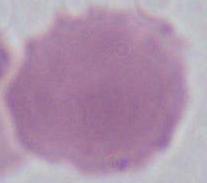
identification = red blood cell
magnification = 1000x
modality = micrograph